State which parasite is depicted.
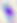

This is Toxoplasma gondii.

Micrograph. Captured at 400x magnification.